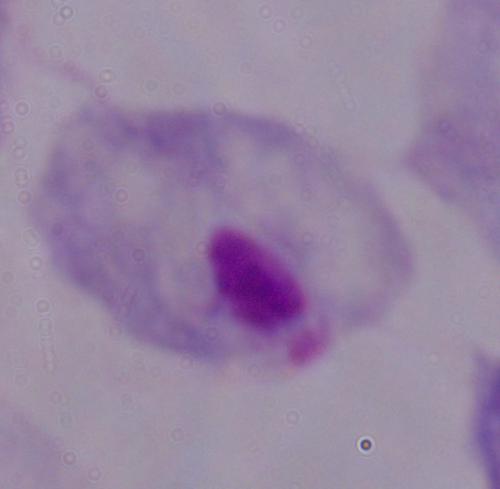
1000x magnification. Micrograph. A trichomonad is shown.